Identify the parasite.
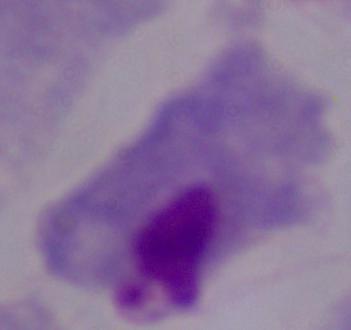

A trichomonad.

Summary:
  - Magnification: 1000x
  - Modality: photomicrograph